State the blood parasite species.
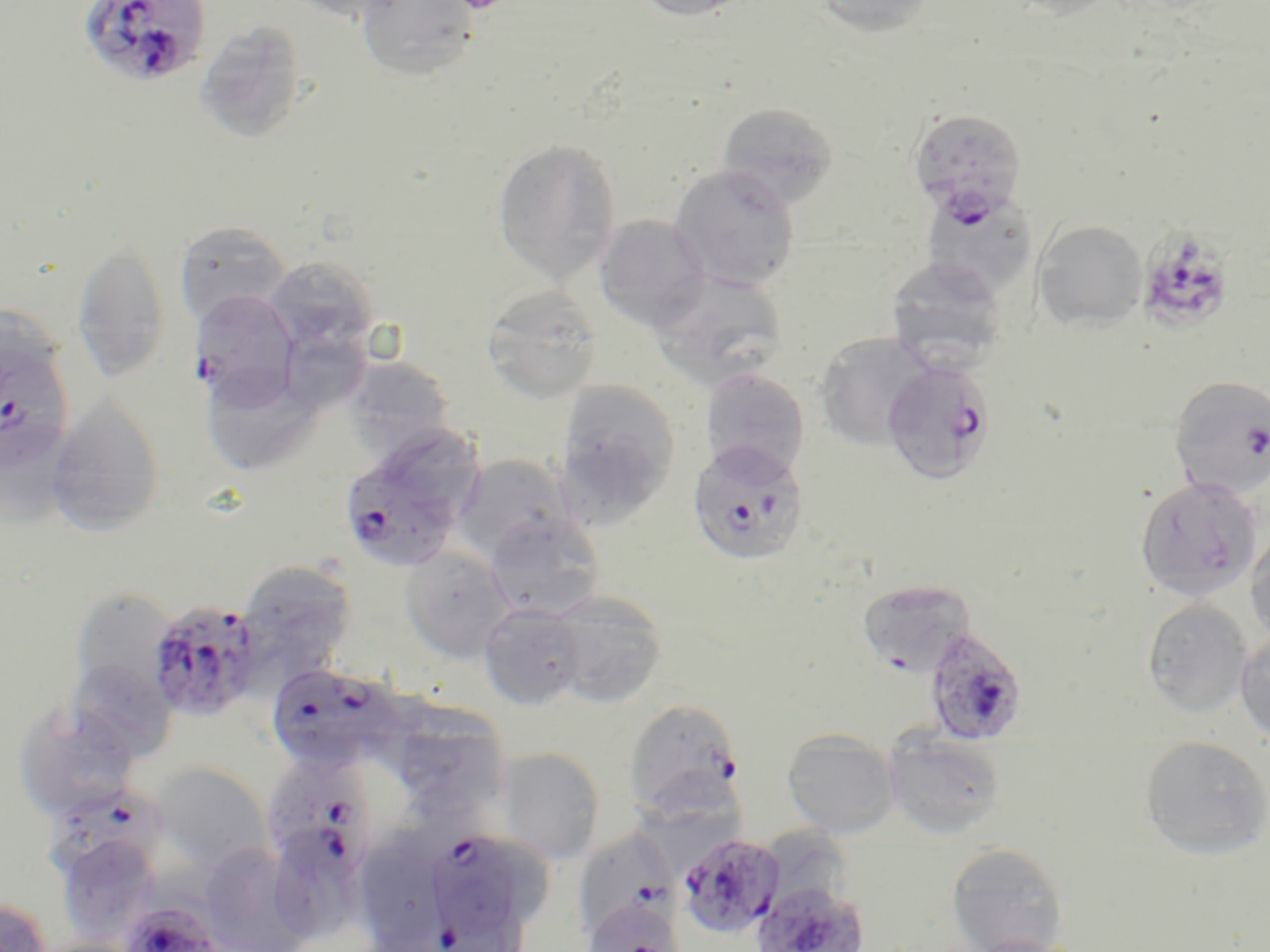
Plasmodium falciparum.

Summary:
  - Coordinate format: approximate bounding boxes as (x1,y1)-(x2,y2) corner pairs in pixels
  - Plasmodium falciparum-infected red blood cell locations: (78,1)-(211,88), (907,107)-(1027,225), (1134,230)-(1239,336), (190,290)-(300,404), (0,321)-(74,474), (880,360)-(997,485), (1169,375)-(1270,500), (688,440)-(809,566), (341,456)-(460,574), (147,599)-(264,723), (923,628)-(1029,747), (264,662)-(402,773), (623,699)-(744,819), (266,763)-(374,883), (48,791)-(164,895), (571,828)-(684,940), (679,833)-(785,939), (432,836)-(519,940), (752,881)-(869,952), (582,896)-(686,952), (119,899)-(224,952)
  - Uninfected red blood cell locations: (279,0)-(412,24), (357,0)-(480,82), (630,0)-(756,22), (814,0)-(938,39), (1001,0)-(1127,20), (193,21)-(307,144), (717,101)-(840,210), (491,138)-(622,287), (668,163)-(801,291), (919,187)-(1040,300), (594,215)-(711,332), (1032,219)-(1149,331), (173,220)-(292,326), (72,241)-(171,382), (263,255)-(380,356), (885,255)-(1009,369), (649,267)-(788,391), (481,285)-(603,404), (814,333)-(935,451), (285,335)-(368,412), (342,354)-(455,462), (699,367)-(810,482), (203,373)-(317,473), (554,379)-(681,521), (46,394)-(166,535), (390,427)-(485,529), (0,428)-(82,534), (452,455)-(575,566), (1134,476)-(1265,603), (483,512)-(605,621), (1245,527)-(1270,650), (399,545)-(516,663), (236,559)-(357,680), (856,578)-(978,676), (68,588)-(178,701), (546,590)-(667,708), (1142,598)-(1254,719), (478,603)-(586,711), (1234,629)-(1270,748), (65,658)-(177,760), (12,701)-(141,821), (403,705)-(505,814), (781,727)-(901,838), (882,728)-(1007,840), (1140,733)-(1270,860), (495,746)-(606,865), (150,762)-(272,874), (637,771)-(745,881), (55,832)-(163,946), (945,841)-(1069,952), (197,842)-(315,951), (364,844)-(443,950), (0,898)-(52,952), (961,935)-(1090,952), (28,937)-(144,952)
  - Stain: May-Grünwald-Giemsa
  - Modality: light microscopy
  - Field of view: one of a larger specimen
  - Magnification: 1000x
  - Preparation: thin blood film
  - Image size: 1270×952 pixels